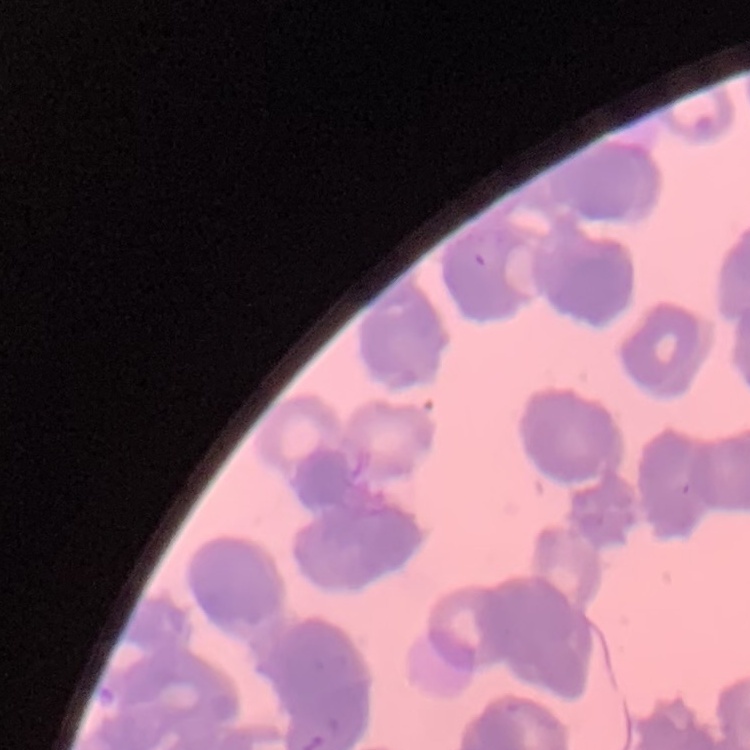

{
  "erythrocyte_morphology": "rouleaux formation",
  "image_type": "square crop of a larger photomicrograph",
  "stain": "Field's or Giemsa",
  "preparation": "thin blood smear"
}